Locate every uninfected red blood cell.
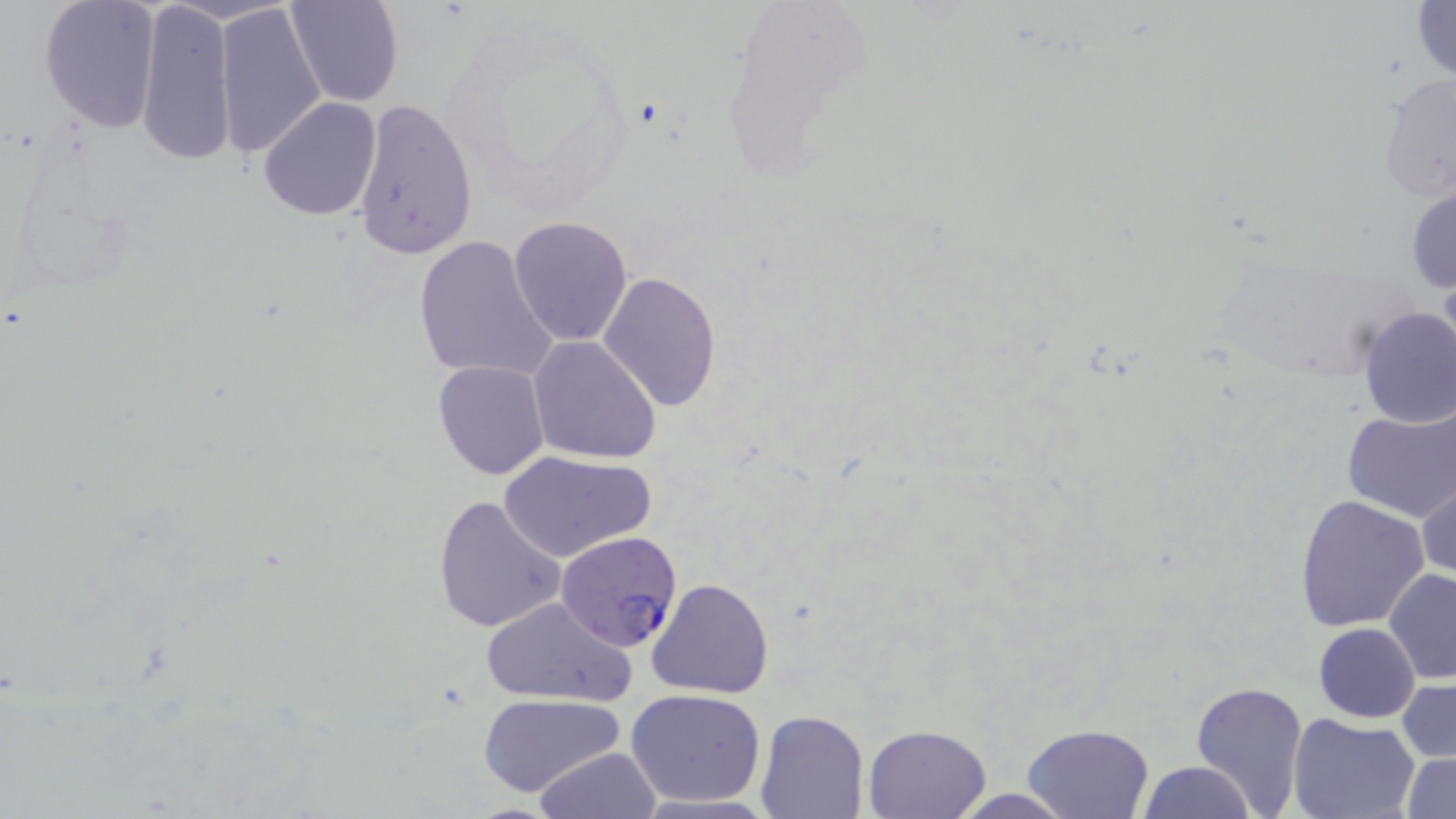

Approximate bounding boxes as (x1, y1, x2, y2) in pixels.
Uninfected red blood cells: (39, 0, 163, 133), (284, 0, 402, 108), (136, 1, 234, 167), (1412, 1, 1456, 83), (215, 3, 327, 159), (1378, 73, 1454, 203), (259, 96, 382, 222), (351, 97, 479, 260), (1406, 182, 1455, 298), (509, 216, 634, 346), (412, 235, 557, 385), (597, 271, 723, 412), (1356, 305, 1456, 430), (528, 336, 660, 464), (432, 360, 551, 480), (1343, 405, 1455, 522), (498, 449, 656, 564), (1415, 474, 1455, 586), (1293, 492, 1431, 632), (432, 494, 567, 634), (1383, 567, 1456, 682), (646, 576, 775, 699), (481, 596, 635, 706), (1314, 623, 1419, 722), (1397, 677, 1455, 766), (1191, 680, 1309, 815), (626, 689, 769, 807), (478, 692, 627, 799), (754, 708, 869, 818), (1289, 714, 1421, 819), (1021, 723, 1155, 819), (862, 724, 990, 818), (534, 747, 662, 818), (1401, 750, 1456, 819), (1137, 760, 1256, 818), (942, 786, 1079, 818).

slide_level_diagnosis: Plasmodium falciparum
preparation: thin blood film
plasmodium_falciparum_infected_red_blood_cell_locations: 'approximate bounding boxes as (x1, y1, x2, y2) in pixels: (558, 528, 684, 651)'
magnification: 1000x
modality: optical microscopy
stain: May-Grünwald-Giemsa
field_of_view: single
image_size: 1456×819 pixels